Identify the parasite.
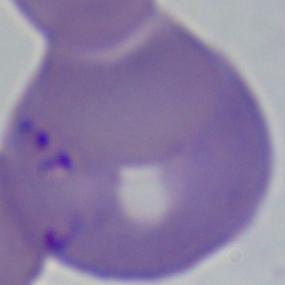
Babesia.

{
  "magnification": "1000x",
  "modality": "micrograph"
}